Describe the morphology of the erythrocytes.
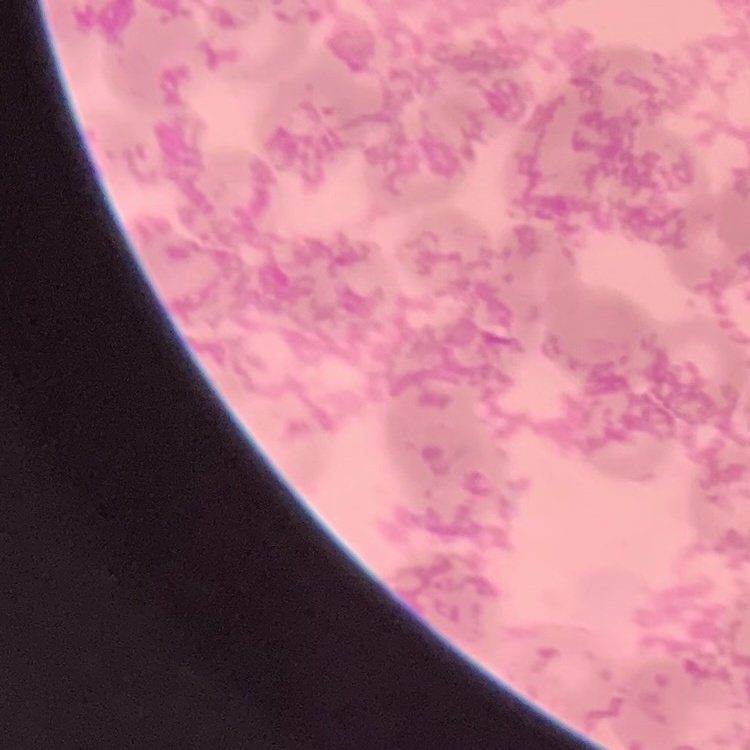

They show rouleaux formation.

Summary:
  - Image type: one tile cut from a larger photomicrograph
  - Preparation: thin blood smear
  - Stain: Field's or Giemsa